Locate platelets.
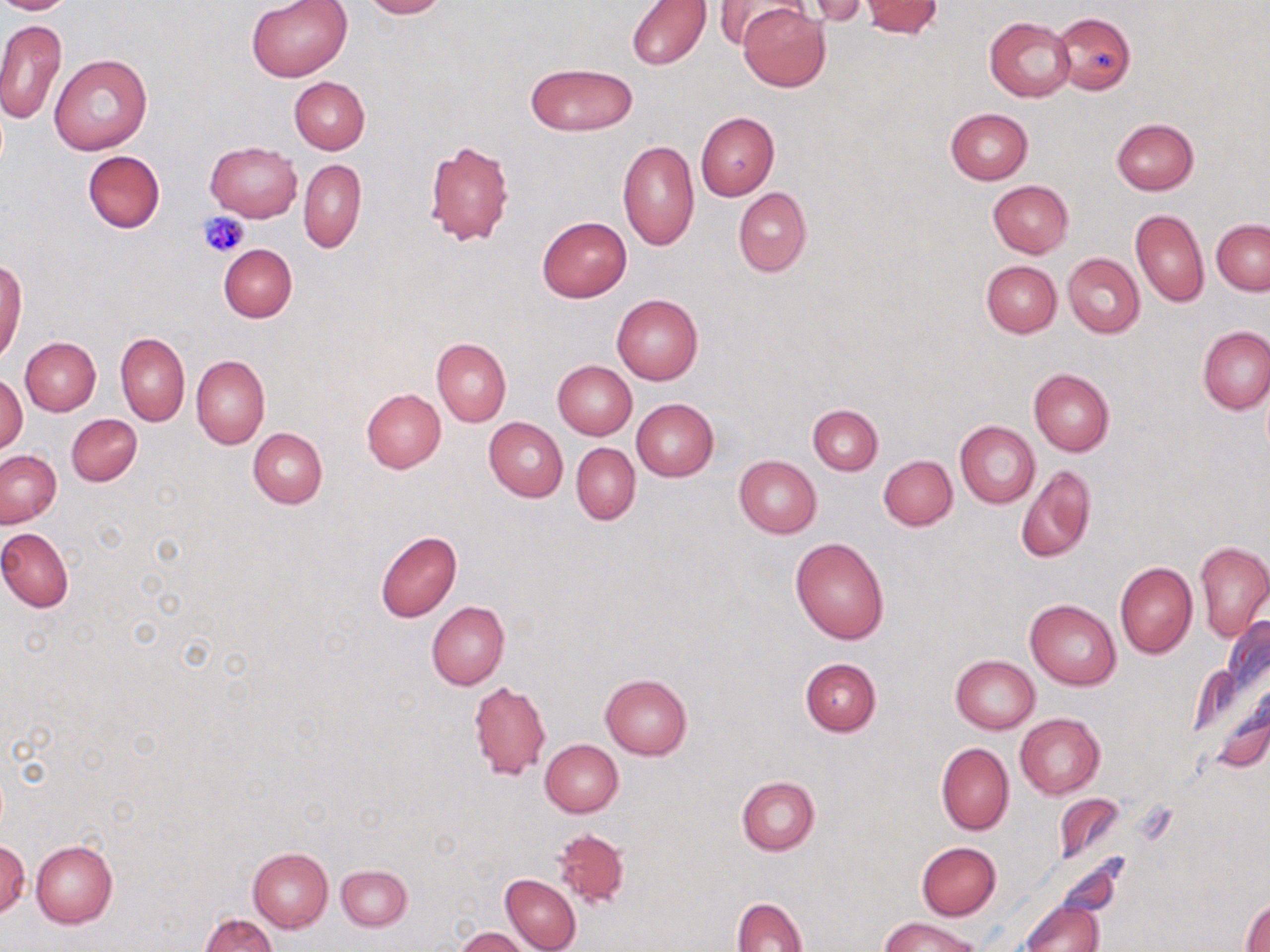

Approximate bounding boxes as [x1, y1, x2, y2] in pixels.
Platelets: [198, 210, 249, 258].

Summary:
  - Uninfected red blood cell locations: [0, 0, 76, 15], [247, 0, 353, 82], [359, 0, 449, 19], [713, 0, 809, 50], [626, 1, 711, 71], [802, 1, 869, 26], [861, 1, 942, 38], [739, 3, 830, 92], [1052, 12, 1134, 94], [984, 16, 1076, 102], [0, 18, 66, 126], [49, 52, 153, 155], [524, 62, 637, 135], [289, 76, 370, 154], [944, 109, 1031, 184], [695, 112, 778, 200], [1111, 118, 1199, 195], [423, 138, 514, 247], [618, 140, 699, 251], [205, 141, 302, 221], [81, 150, 164, 234], [298, 159, 367, 253], [988, 180, 1074, 257], [733, 187, 812, 277], [1131, 209, 1208, 308], [537, 216, 632, 301], [1212, 220, 1269, 295], [218, 244, 297, 322], [1063, 253, 1145, 337], [0, 257, 26, 364], [980, 259, 1062, 337], [611, 294, 703, 385], [1198, 327, 1269, 415], [115, 332, 190, 426], [19, 337, 100, 416], [432, 337, 511, 427], [192, 355, 269, 448], [552, 361, 636, 440], [1028, 368, 1115, 455], [1, 374, 27, 454], [360, 388, 445, 473], [632, 399, 718, 481], [808, 404, 883, 475], [66, 413, 141, 486], [484, 417, 568, 502], [954, 421, 1039, 508], [249, 428, 328, 508], [571, 442, 640, 524], [1, 450, 61, 527], [734, 456, 822, 538], [878, 456, 956, 530], [1016, 463, 1096, 563], [0, 526, 74, 612], [375, 529, 461, 623], [790, 537, 890, 643], [1195, 541, 1270, 642], [1114, 561, 1196, 658], [1026, 598, 1122, 690], [427, 601, 509, 690], [950, 655, 1039, 733], [800, 657, 881, 736], [600, 674, 692, 760], [470, 681, 550, 780], [1016, 713, 1104, 799], [540, 739, 623, 817], [936, 743, 1014, 835], [736, 777, 819, 855], [1055, 793, 1124, 863], [553, 826, 630, 909], [1, 837, 29, 919], [31, 841, 117, 928], [915, 841, 1001, 920], [248, 847, 332, 932], [336, 865, 412, 931], [500, 874, 581, 952], [732, 896, 806, 951], [1242, 898, 1269, 951], [1019, 901, 1102, 952], [200, 914, 276, 951], [880, 916, 980, 952], [455, 928, 530, 952]
  - Slide-level diagnosis: no evidence of blood parasites
  - Stain: May-Grünwald-Giemsa
  - Image size: 1270×952 pixels
  - Preparation: thin blood film
  - Field of view: single
  - Magnification: 1000x
  - Modality: light microscopy